Locate every blood parasite and identify its species.
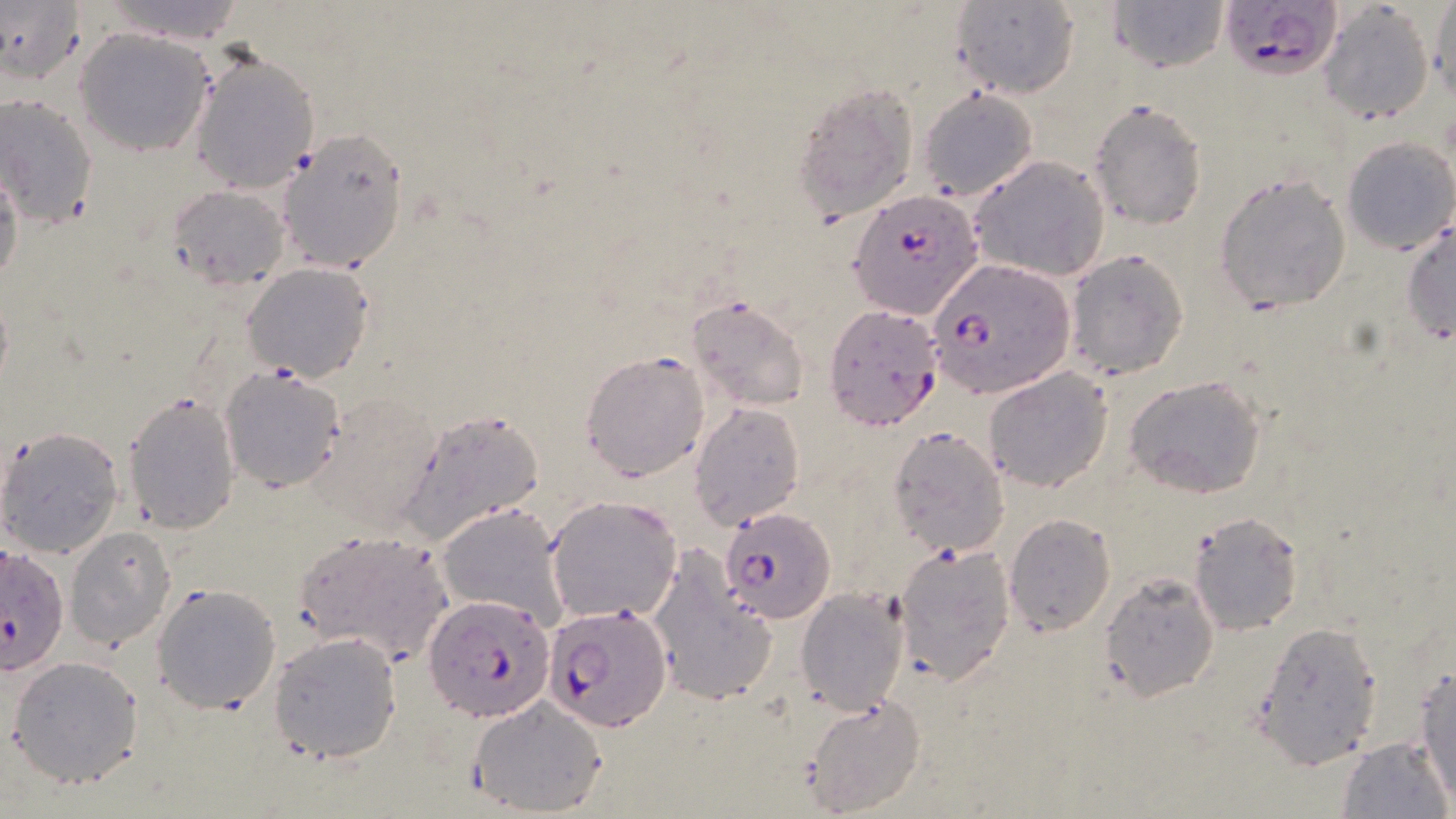

Approximate bounding boxes as [x1, y1, x2, y2] in pixels.
Plasmodium falciparum-infected red blood cells: [1221, 0, 1345, 81], [851, 188, 983, 321], [927, 257, 1076, 397], [823, 305, 943, 431], [719, 507, 836, 623], [2, 542, 69, 680], [425, 595, 555, 718], [542, 604, 671, 732].
No Plasmodium ovale, Plasmodium malariae, Plasmodium vivax, Babesia divergens, or Trypanosoma brucei observed.

slide-level diagnosis = Plasmodium falciparum
modality = light microscopy
stain = May-Grünwald-Giemsa
magnification = 1000x
image size = 1456×819 pixels
uninfected red blood cell locations = approximate bounding boxes as [x1, y1, x2, y2] in pixels: [1, 0, 85, 84], [94, 0, 251, 44], [1428, 0, 1456, 107], [948, 1, 1080, 97], [1107, 1, 1231, 73], [1318, 3, 1434, 124], [74, 28, 215, 156], [190, 48, 319, 195], [793, 82, 920, 218], [916, 88, 1037, 202], [0, 94, 99, 228], [1088, 99, 1210, 229], [276, 128, 411, 272], [1341, 135, 1455, 255], [970, 155, 1110, 282], [0, 165, 24, 290], [1214, 170, 1352, 315], [167, 184, 291, 289], [1401, 218, 1455, 348], [1064, 248, 1189, 379], [242, 262, 376, 383], [686, 296, 810, 412], [579, 349, 712, 483], [219, 364, 347, 492], [983, 367, 1113, 493], [1123, 374, 1266, 499], [122, 391, 243, 535], [689, 402, 806, 530], [398, 410, 544, 541], [0, 426, 123, 559], [885, 426, 1010, 557], [545, 495, 683, 624], [436, 503, 570, 631], [1188, 511, 1303, 633], [1004, 513, 1116, 635], [66, 527, 175, 649], [289, 529, 455, 667], [892, 540, 1016, 686], [646, 547, 776, 708], [1098, 573, 1220, 702], [152, 584, 282, 714], [796, 587, 910, 713], [1252, 620, 1383, 766], [270, 632, 401, 761], [8, 655, 145, 789], [1411, 658, 1455, 803], [804, 694, 924, 815], [467, 695, 606, 816], [1338, 737, 1452, 819]
preparation = thin blood smear
field of view = one of a larger specimen